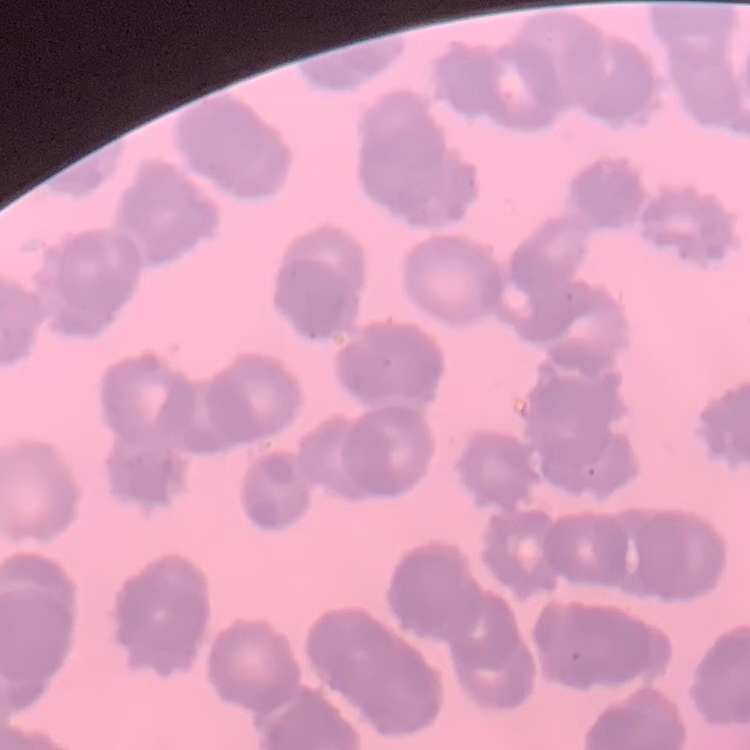

red blood cell morphology = rouleaux formation
stain = Field's or Giemsa
preparation = thin blood film
image type = square crop of a larger photomicrograph